Assess this cell for malaria.
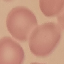

Uninfected.

Thin smear of blood. Giemsa stain. Acquired by smartphone through the microscope eyepiece. Cell patch, automatically extracted from a larger field of view and resized to 64 × 64 pixels.